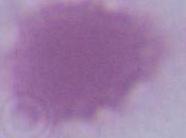

Micrograph. A red blood cell is seen. 1000x magnification.